Assess for Plasmodium parasites.
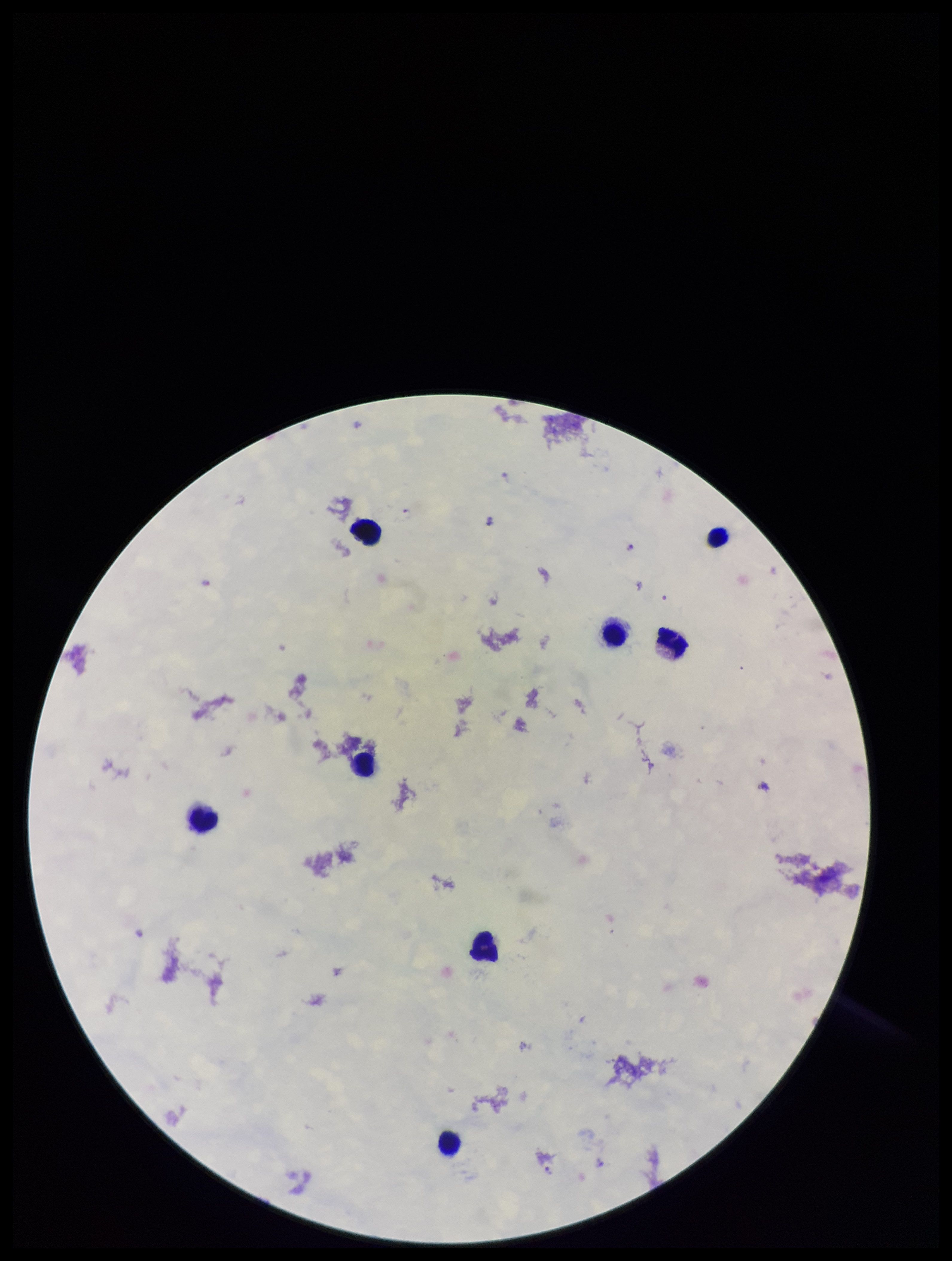
Detected.

Summary:
  - Leukocyte count: 8
  - Field of view: single
  - Parasite count: 7
  - Species reported for this patient: Plasmodium falciparum
  - Capture: smartphone photograph through the microscope eyepiece
  - Image size: 952×1261 pixels
  - Patient malaria status: positive
  - Stain: Giemsa
  - Preparation: thick smear